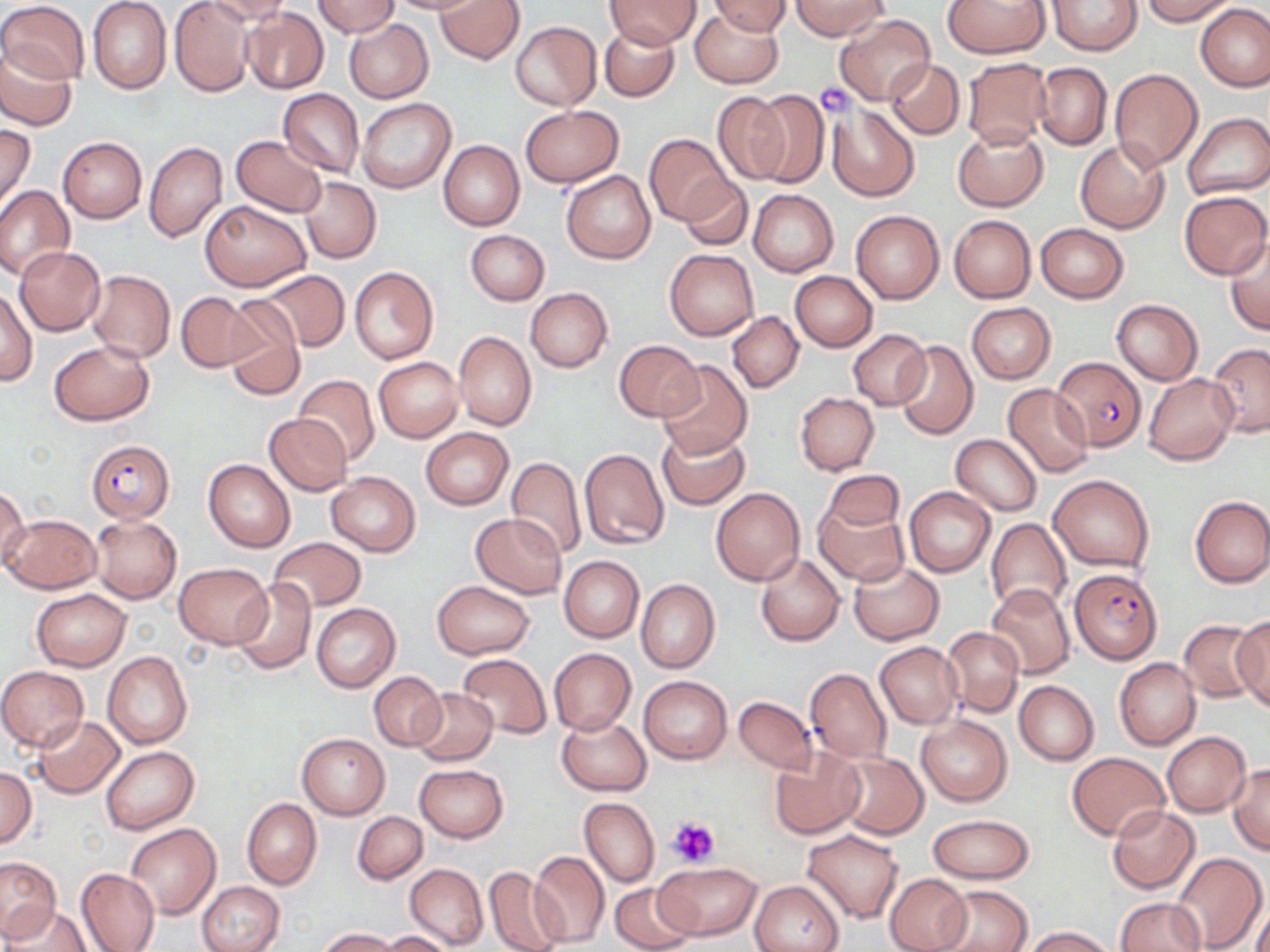

slide_level_diagnosis: Plasmodium falciparum
preparation: thin blood film
stain: May-Grünwald-Giemsa
magnification: 1000x
platelet_locations: 'approximate bounding boxes as (x1, y1, x2, y2) in pixels: (813, 83, 857, 116), (666, 816, 720, 868)'
field_of_view: one of a larger specimen
uninfected_red_blood_cell_locations: 'approximate bounding boxes as (x1, y1, x2, y2) in pixels: (171, 0, 255, 97), (204, 0, 290, 30), (385, 0, 480, 16), (435, 0, 523, 64), (944, 0, 1049, 58), (1046, 0, 1142, 56), (1139, 0, 1237, 25), (0, 1, 89, 87), (87, 1, 172, 94), (312, 1, 399, 37), (604, 1, 699, 49), (704, 1, 789, 37), (791, 1, 888, 40), (1196, 4, 1270, 92), (690, 6, 782, 88), (241, 7, 328, 94), (835, 14, 934, 106), (343, 18, 433, 102), (511, 21, 601, 110), (599, 25, 679, 102), (1, 43, 76, 129), (961, 57, 1054, 149), (885, 58, 965, 138), (1032, 62, 1112, 150), (1109, 68, 1202, 171), (278, 87, 365, 179), (749, 89, 829, 188), (712, 91, 792, 185), (357, 98, 457, 194), (827, 103, 919, 201), (519, 106, 624, 187), (1181, 113, 1270, 200), (0, 124, 36, 211), (953, 126, 1047, 211), (644, 134, 733, 224), (232, 135, 327, 216), (58, 136, 147, 223), (1074, 140, 1168, 233), (145, 141, 227, 244), (438, 141, 524, 230), (561, 170, 656, 264), (299, 176, 382, 264), (679, 176, 752, 251), (0, 185, 75, 281), (749, 189, 838, 277), (1179, 191, 1270, 279), (201, 199, 311, 292), (851, 210, 944, 304), (948, 215, 1035, 302), (1036, 223, 1128, 303), (466, 229, 549, 305), (1225, 235, 1270, 335), (15, 246, 106, 336), (664, 248, 759, 341), (349, 267, 438, 364), (86, 269, 175, 362), (257, 270, 350, 351), (789, 271, 878, 351), (0, 286, 37, 386), (525, 287, 612, 372), (177, 292, 261, 372), (222, 298, 306, 400), (1112, 299, 1203, 385), (966, 303, 1056, 383), (727, 311, 804, 393), (453, 330, 537, 430), (848, 330, 932, 409), (892, 339, 978, 439), (50, 340, 154, 425), (614, 341, 705, 420), (1206, 342, 1270, 436), (373, 357, 462, 443), (657, 360, 752, 458), (1143, 372, 1238, 465), (294, 375, 379, 461), (1003, 383, 1094, 477), (794, 392, 879, 475), (263, 413, 352, 495), (420, 427, 514, 509), (657, 428, 750, 510), (950, 434, 1043, 515), (579, 447, 670, 550), (506, 456, 587, 558), (204, 458, 295, 552), (821, 470, 903, 535), (325, 471, 421, 555), (1048, 473, 1155, 572), (0, 485, 29, 574), (710, 488, 805, 585), (904, 488, 994, 577), (1190, 495, 1270, 588), (813, 499, 908, 587), (471, 512, 565, 598), (1, 514, 101, 593), (91, 516, 182, 603), (985, 518, 1072, 614), (267, 536, 367, 613), (755, 553, 845, 646), (559, 556, 643, 642), (847, 560, 944, 644), (173, 562, 273, 648), (232, 578, 315, 674), (636, 579, 720, 672), (431, 581, 535, 659), (986, 583, 1076, 678), (31, 589, 131, 671), (311, 602, 400, 691), (1232, 618, 1270, 710), (1179, 620, 1265, 702), (941, 625, 1023, 718), (875, 642, 963, 729), (549, 648, 635, 735), (103, 651, 193, 751), (458, 654, 551, 739), (1114, 657, 1201, 750), (0, 666, 89, 752), (805, 668, 892, 764), (369, 671, 446, 751), (639, 675, 732, 764), (1013, 680, 1099, 764), (410, 687, 497, 765), (733, 695, 816, 774), (31, 715, 125, 799), (557, 716, 651, 795), (917, 716, 1012, 805), (1162, 731, 1250, 817), (297, 732, 391, 819), (102, 745, 199, 834), (769, 748, 866, 840), (1067, 752, 1169, 841), (833, 753, 928, 840), (1228, 763, 1270, 854), (414, 764, 509, 843), (0, 766, 37, 848), (579, 797, 659, 888), (242, 798, 321, 890), (1106, 804, 1200, 893), (352, 811, 427, 884), (927, 813, 1034, 884), (126, 822, 221, 918), (803, 829, 903, 925), (529, 849, 609, 946), (1170, 851, 1266, 952), (0, 856, 60, 943), (655, 861, 761, 941), (405, 863, 487, 948), (75, 867, 160, 952), (483, 867, 568, 952), (884, 872, 972, 952), (609, 879, 699, 952), (752, 879, 844, 952), (1239, 879, 1266, 952), (198, 880, 285, 952), (929, 885, 1033, 952), (1250, 889, 1270, 952), (1114, 897, 1207, 952), (7, 903, 90, 952), (1023, 926, 1117, 952), (318, 928, 400, 951), (380, 931, 455, 952)'
image_size: 1270×952 pixels
modality: optical microscopy
plasmodium_falciparum_infected_red_blood_cell_locations: 'approximate bounding boxes as (x1, y1, x2, y2) in pixels: (1053, 356, 1147, 450), (88, 440, 175, 523), (1069, 567, 1161, 664)'